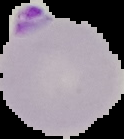
malaria status = parasitized
image type = segmented cell region on a black background
preparation = thin blood smear
image size = 124×139 pixels